Report the malaria status of this cell.
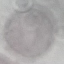
It is uninfected.

preparation = thin smear
stain = Giemsa
image type = cell patch, automatically extracted from a larger field of view and resized to 64 × 64 pixels
capture = smartphone through the microscope eyepiece